Give the extent of all Plasmodium falciparum-infected red blood cells.
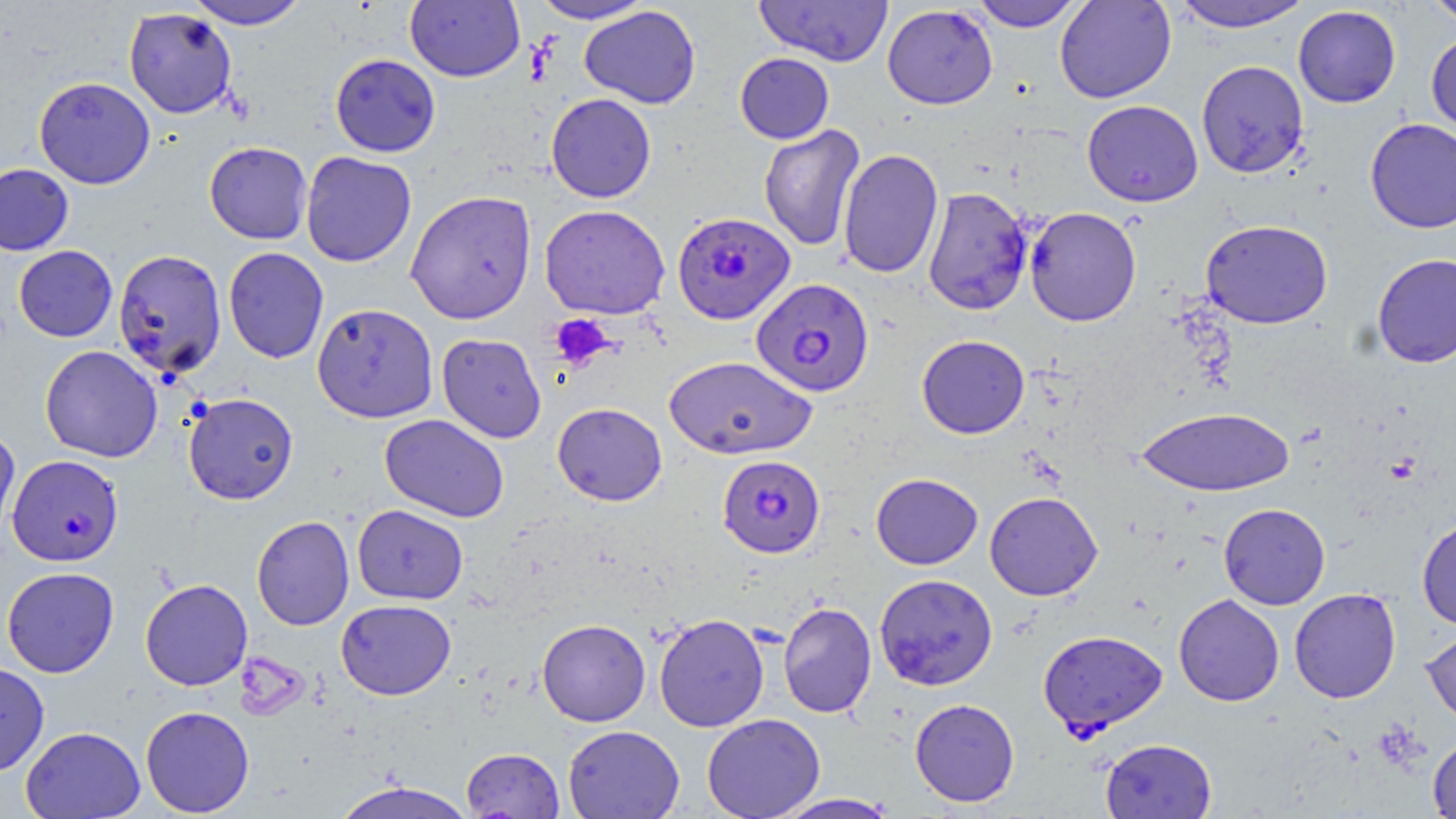

Approximate bounding boxes as (x1, y1, x2, y2) in pixels.
Plasmodium falciparum-infected red blood cells: (672, 211, 796, 325), (751, 277, 875, 397), (7, 454, 124, 566), (717, 454, 825, 558), (1038, 630, 1168, 736).

Platelet locations: (549, 314, 615, 372). Uninfected red blood cell locations: (184, 0, 310, 30), (530, 0, 654, 24), (754, 0, 893, 66), (969, 0, 1084, 31), (1054, 0, 1176, 103), (1169, 0, 1313, 33), (1423, 0, 1456, 26), (405, 1, 525, 82), (579, 5, 701, 109), (882, 5, 998, 109), (1293, 5, 1401, 108), (123, 7, 237, 119), (1426, 30, 1456, 139), (735, 52, 834, 144), (330, 53, 441, 157), (1196, 60, 1309, 178), (34, 77, 156, 189), (546, 93, 656, 203), (1082, 100, 1203, 207), (1364, 118, 1456, 233), (758, 124, 866, 251), (204, 141, 313, 244), (838, 148, 944, 279), (301, 151, 417, 267), (0, 162, 75, 256), (923, 186, 1033, 316), (405, 190, 537, 324), (539, 204, 670, 319), (1025, 207, 1142, 326), (1200, 219, 1333, 329), (13, 245, 118, 342), (223, 246, 329, 364), (113, 249, 227, 380), (1371, 252, 1456, 368), (312, 302, 438, 422), (436, 333, 547, 444), (917, 335, 1029, 438), (40, 345, 163, 463), (663, 355, 817, 459), (183, 392, 299, 505), (552, 402, 667, 506), (1136, 405, 1295, 496), (380, 413, 509, 522), (0, 426, 20, 542), (870, 473, 983, 570), (984, 491, 1103, 601), (1218, 503, 1331, 610), (352, 504, 468, 605), (251, 515, 355, 631), (1416, 517, 1456, 630), (1, 567, 119, 678), (874, 573, 998, 691), (140, 578, 253, 691), (1289, 588, 1402, 703), (1174, 594, 1285, 706), (336, 599, 456, 700), (778, 601, 877, 719), (654, 613, 770, 732), (537, 619, 650, 727), (1421, 627, 1456, 729), (0, 661, 50, 777), (910, 698, 1020, 807), (140, 705, 255, 816), (702, 713, 825, 819), (20, 725, 145, 818), (563, 725, 685, 818), (1427, 733, 1456, 818), (1100, 737, 1216, 818), (461, 747, 565, 818), (329, 779, 480, 819), (773, 793, 899, 818). Slide-level diagnosis: Plasmodium falciparum. One field of a larger specimen. Thin blood smear. May-Grünwald-Giemsa stain. Image is 1456×819 pixels. Light microscopy. Captured at 1000x magnification.